Assess this cell for malaria.
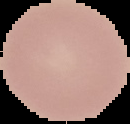

Uninfected.

Segmented cell region on a black background. From a thin blood film. Image is 130×124 pixels.